Assess this cell for malaria.
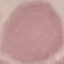
It is uninfected.

preparation = thin smear
stain = Giemsa
image type = automatically extracted cell patch, resized to 64 × 64 pixels
capture = smartphone camera at the microscope eyepiece